Evaluate for malaria.
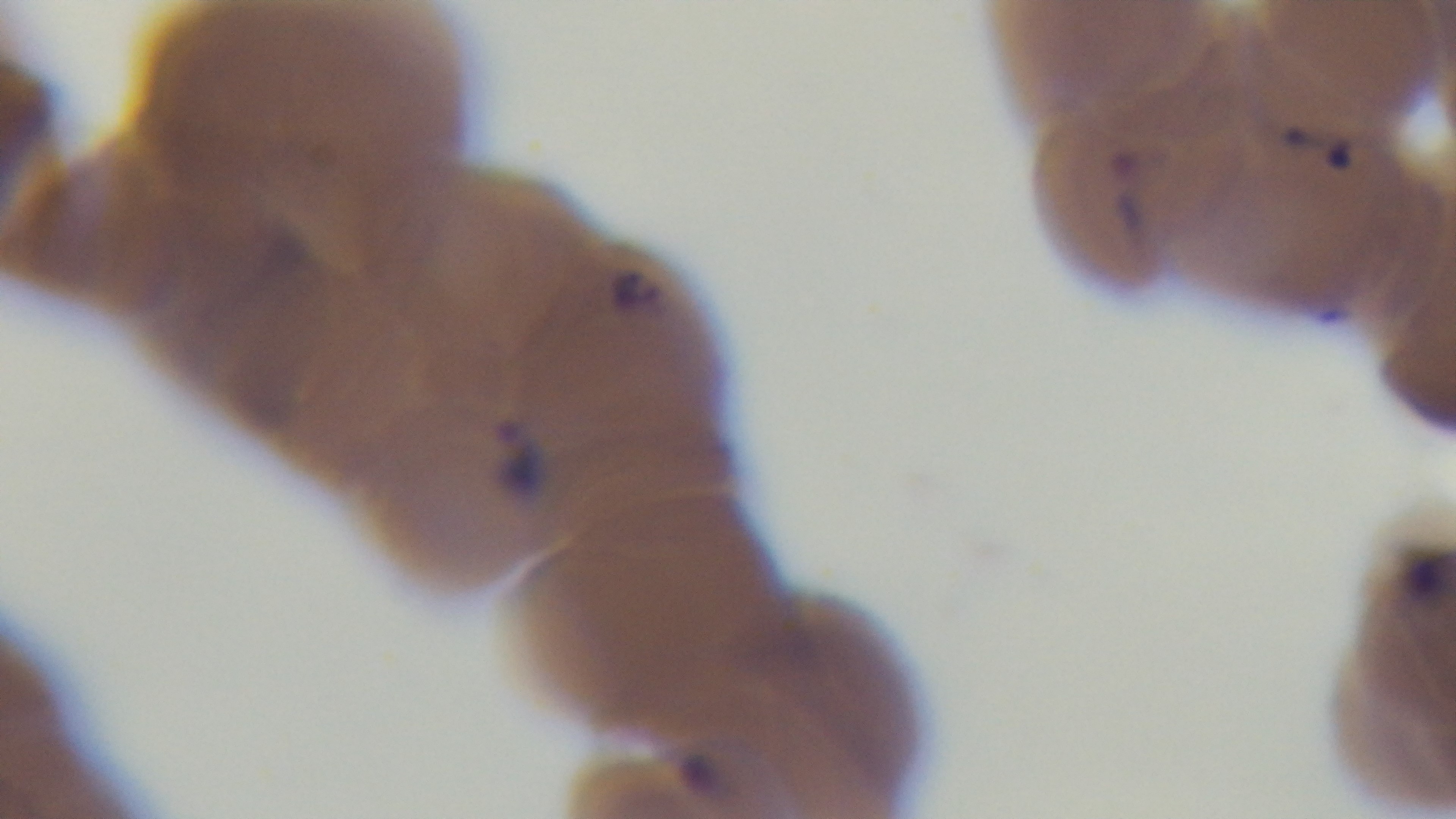

Positive.

Single field of view. Mounted 4K digital camera. Preparation: thin. Photomicrograph. Oil-immersion objective, 100x. Giemsa stain.